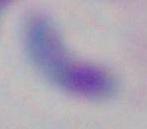

identification = Toxoplasma gondii
modality = photomicrograph
magnification = 1000x